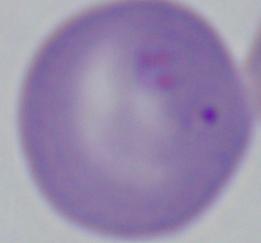
modality: micrograph
magnification: 1000x
identification: Babesia